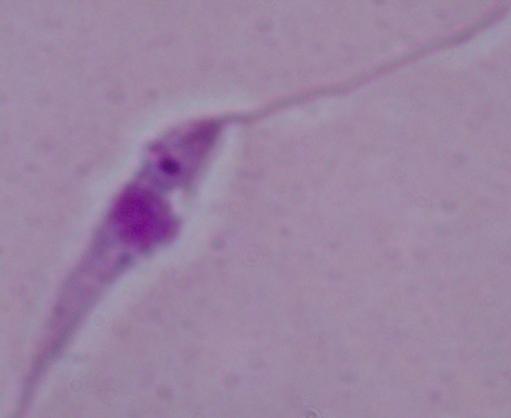

identification: Leishmania
modality: photomicrograph
magnification: 1000x